Name the parasite shown.
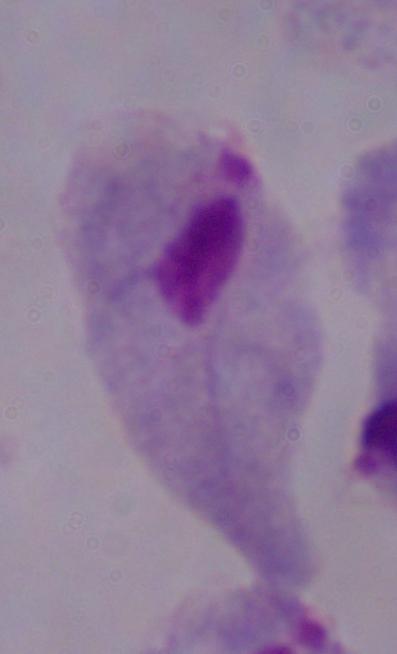
This is a trichomonad.

Photomicrograph. Captured at 1000x magnification.